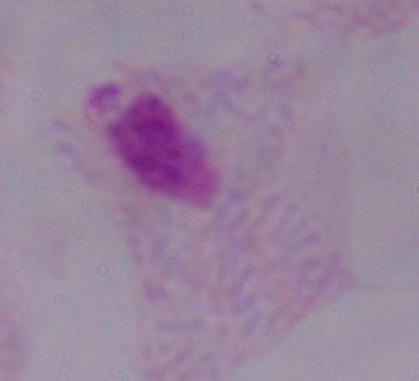
magnification = 1000x
modality = micrograph
identification = trichomonad